Name the parasite shown.
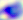

Toxoplasma gondii.

modality: micrograph
magnification: 400x